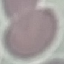

Malaria status: uninfected. Thin blood film. Giemsa stain. Automatically extracted cell patch, resized to 64 × 64 pixels. Acquired by smartphone through the microscope eyepiece.